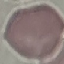
Result: no malaria parasites seen. Cell patch, automatically extracted from a larger field of view and resized to 64 × 64 pixels. Acquired by smartphone through the microscope eyepiece. Thin blood film. Giemsa-stained preparation.